Classify this cell by malaria status.
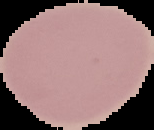

It is uninfected.

Summary:
  - Image size: 154×130 pixels
  - Preparation: thin blood film
  - Image type: cell region segmented out of the field of view; surrounding area masked to black